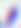

Summary:
  - Identification: Toxoplasma gondii
  - Magnification: 400x
  - Modality: photomicrograph